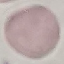

malaria_status: uninfected
image_type: automatically extracted cell patch, resized to 64 × 64 pixels
capture: smartphone camera at the microscope eyepiece
stain: Giemsa
preparation: thin blood film